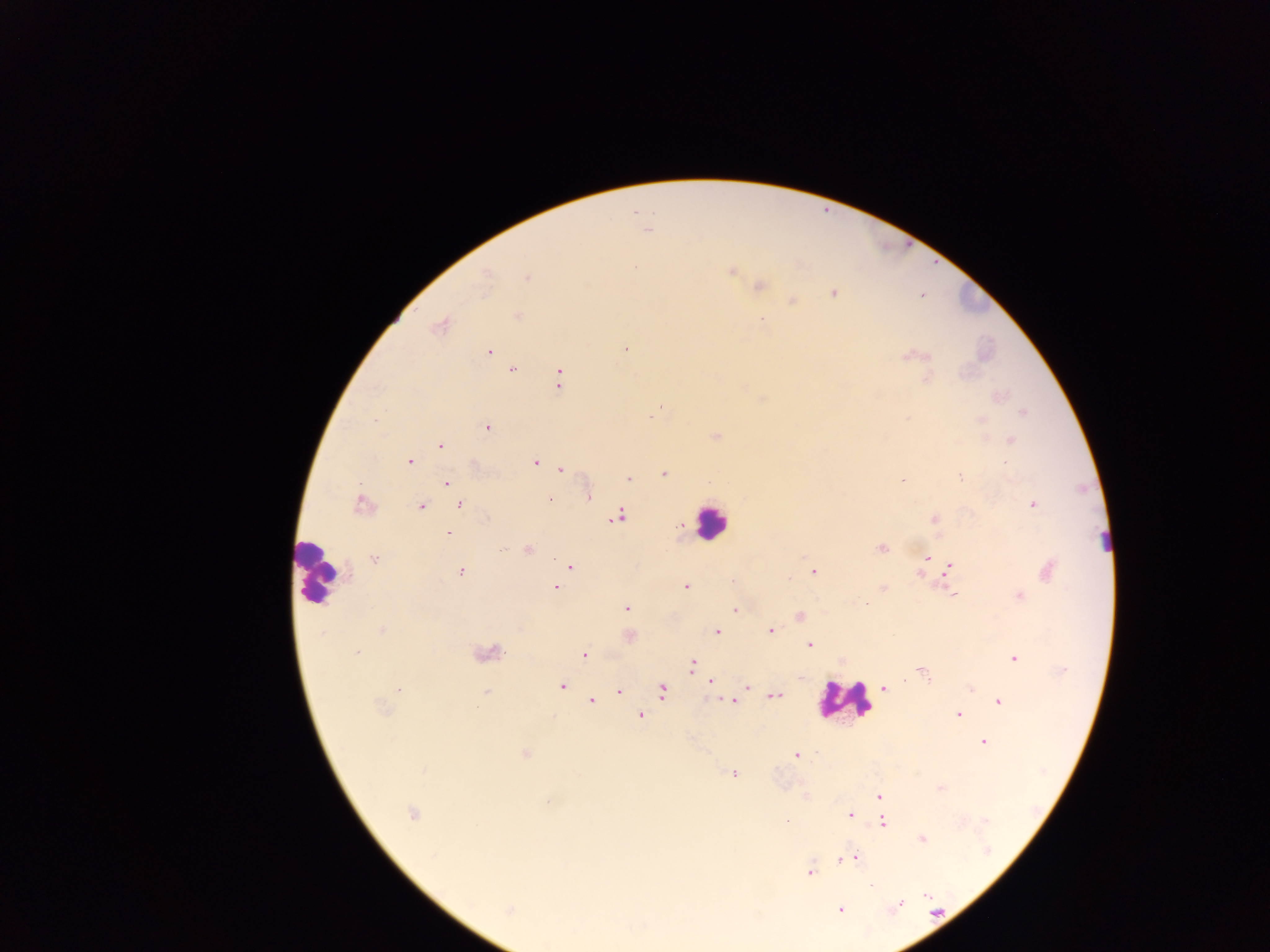

leukocyte locations = approximate centers as x y in pixels: 711 521; 1104 541; 318 572; 844 700
malaria parasite locations = approximate centers as x y in pixels: 646 230; 634 267; 732 272; 486 276; 526 278; 760 286; 833 293; 921 295; 792 300; 518 317; 761 319; 440 326; 625 349; 488 352; 906 356; 512 370; 558 379; 926 379; 661 406; 1022 413; 650 417; 980 420; 375 421; 488 427; 716 436; 1011 441; 440 446; 409 461; 535 462; 561 468; 664 474; 960 476; 628 479; 902 481; 446 483; 588 498; 549 500; 361 504; 460 505; 1032 505; 421 507; 618 517; 934 519; 448 533; 503 548; 881 548; 528 549; 927 557; 374 558; 570 566; 950 566; 1049 570; 461 571; 813 571; 732 580; 685 586; 555 588; 883 588; 953 595; 1019 595; 867 603; 626 609; 735 610; 799 616; 382 630; 771 631; 717 632; 630 635; 810 644; 357 652; 489 653; 584 655; 1014 659; 691 665; 922 672; 710 682; 561 686; 747 686; 884 688; 399 689; 970 689; 619 691; 662 691; 486 692; 775 695; 591 700; 732 701; 999 702; 382 709; 957 715; 641 716; 983 743; 525 754; 796 756; 423 770; 733 774; 879 796; 548 801; 412 814; 850 815; 883 823; 922 839; 852 857; 842 859; 809 873; 871 885; 927 896; 898 905; 508 910; 840 910
capture = mobile-phone photograph through a microscope
country = Ghana
preparation = thick blood smear
image size = 1270×952 pixels
field of view = single